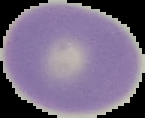
preparation: thin blood film
image_type: cell region segmented out of the field of view; surrounding area masked to black
result: no Plasmodium parasites detected
image_size: 145×118 pixels